Give the extent of all Plasmodium falciparum-infected red blood cells.
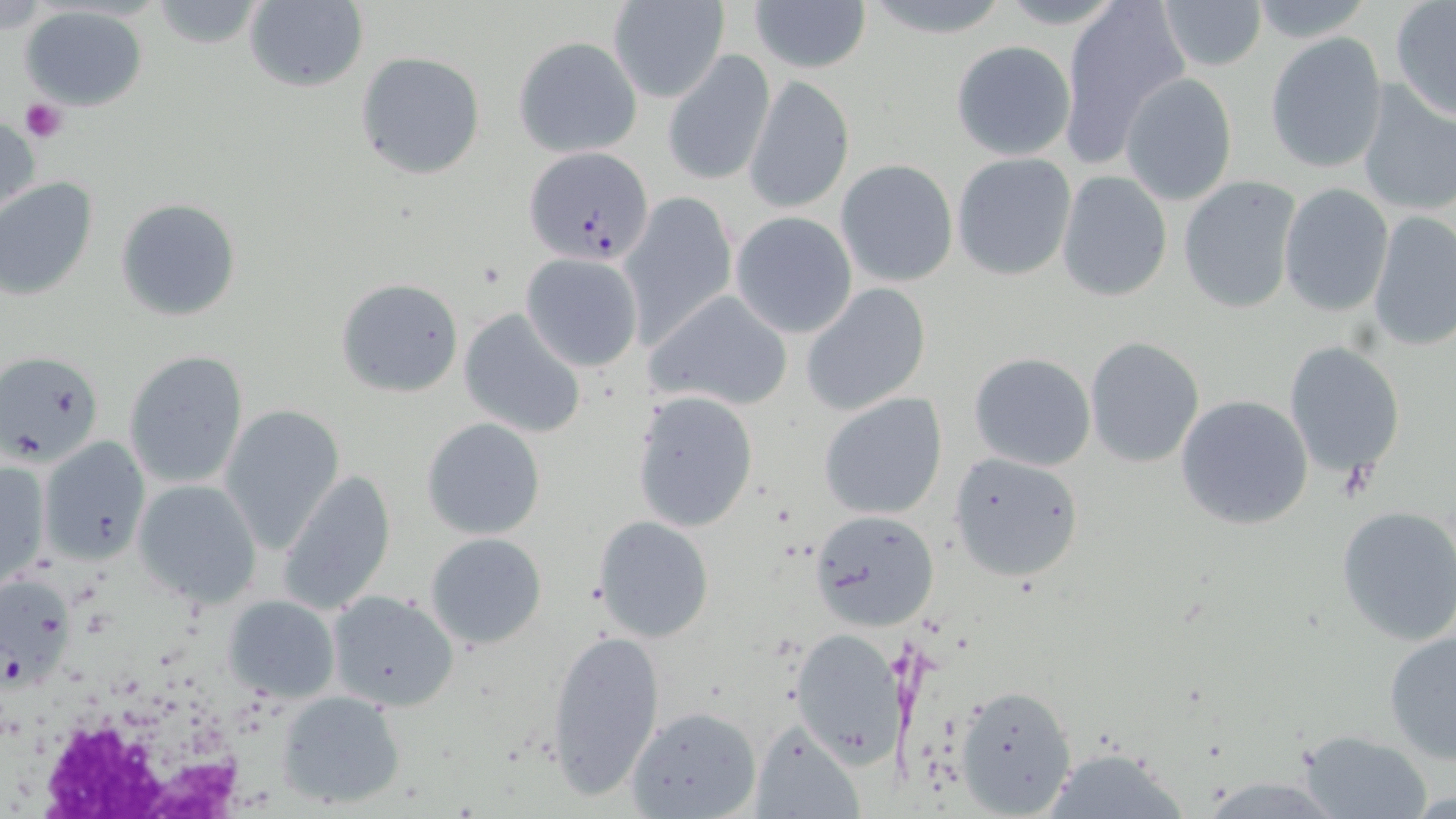

Approximate bounding boxes as (x1,y1)-(x2,y2) corner pairs in pixels.
Plasmodium falciparum-infected red blood cells: (523,144)-(656,266), (0,571)-(77,694).

slide-level diagnosis = Plasmodium falciparum
platelet locations = approximate bounding boxes as (x1,y1)-(x2,y2) corner pairs in pixels: (20,98)-(66,143)
preparation = thin blood smear
field of view = single
uninfected red blood cell locations = approximate bounding boxes as (x1,y1)-(x2,y2) corner pairs in pixels: (859,0)-(1012,38), (996,0)-(1130,27), (1058,0)-(1189,165), (244,1)-(369,91), (751,1)-(870,75), (1156,1)-(1267,72), (148,2)-(264,49), (609,2)-(727,105), (1389,2)-(1456,122), (20,5)-(150,113), (1265,33)-(1388,173), (512,35)-(642,157), (950,40)-(1074,162), (662,49)-(775,187), (355,51)-(486,179), (1120,73)-(1238,204), (743,76)-(856,213), (1354,81)-(1456,218), (0,115)-(40,219), (951,152)-(1076,281), (835,159)-(958,287), (1057,171)-(1172,302), (1177,175)-(1301,315), (0,178)-(97,299), (1280,183)-(1394,317), (618,192)-(737,345), (114,198)-(241,322), (1368,210)-(1456,353), (730,212)-(858,337), (520,253)-(644,371), (336,277)-(465,398), (800,284)-(931,415), (645,290)-(792,413), (459,307)-(586,438), (1084,336)-(1206,469), (1284,340)-(1406,479), (123,349)-(250,489), (1,351)-(106,468), (969,351)-(1096,471), (631,390)-(759,533), (818,392)-(947,518), (1174,393)-(1315,530), (220,404)-(345,552), (421,417)-(546,539), (39,438)-(149,563), (948,452)-(1082,582), (0,459)-(49,587), (276,468)-(399,615), (131,478)-(261,606), (1336,504)-(1456,646), (809,508)-(940,632), (593,515)-(714,642), (424,532)-(548,649), (326,590)-(459,712), (222,595)-(340,704), (544,627)-(665,800), (1383,627)-(1456,763), (790,628)-(903,768), (953,682)-(1079,817), (277,689)-(407,808), (626,704)-(762,818), (749,721)-(866,819), (1296,729)-(1433,818), (1039,751)-(1190,819)
stain = May-Grünwald-Giemsa
image size = 1456×819 pixels
white blood cell locations = approximate bounding boxes as (x1,y1)-(x2,y2) corner pairs in pixels: (5,684)-(273,819)
magnification = 1000x
modality = light microscopy